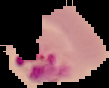 From a thin blood smear. Malaria status: parasitized. Cell region segmented out of the field of view; the surrounding area is masked to black. Image is 109×88 pixels.